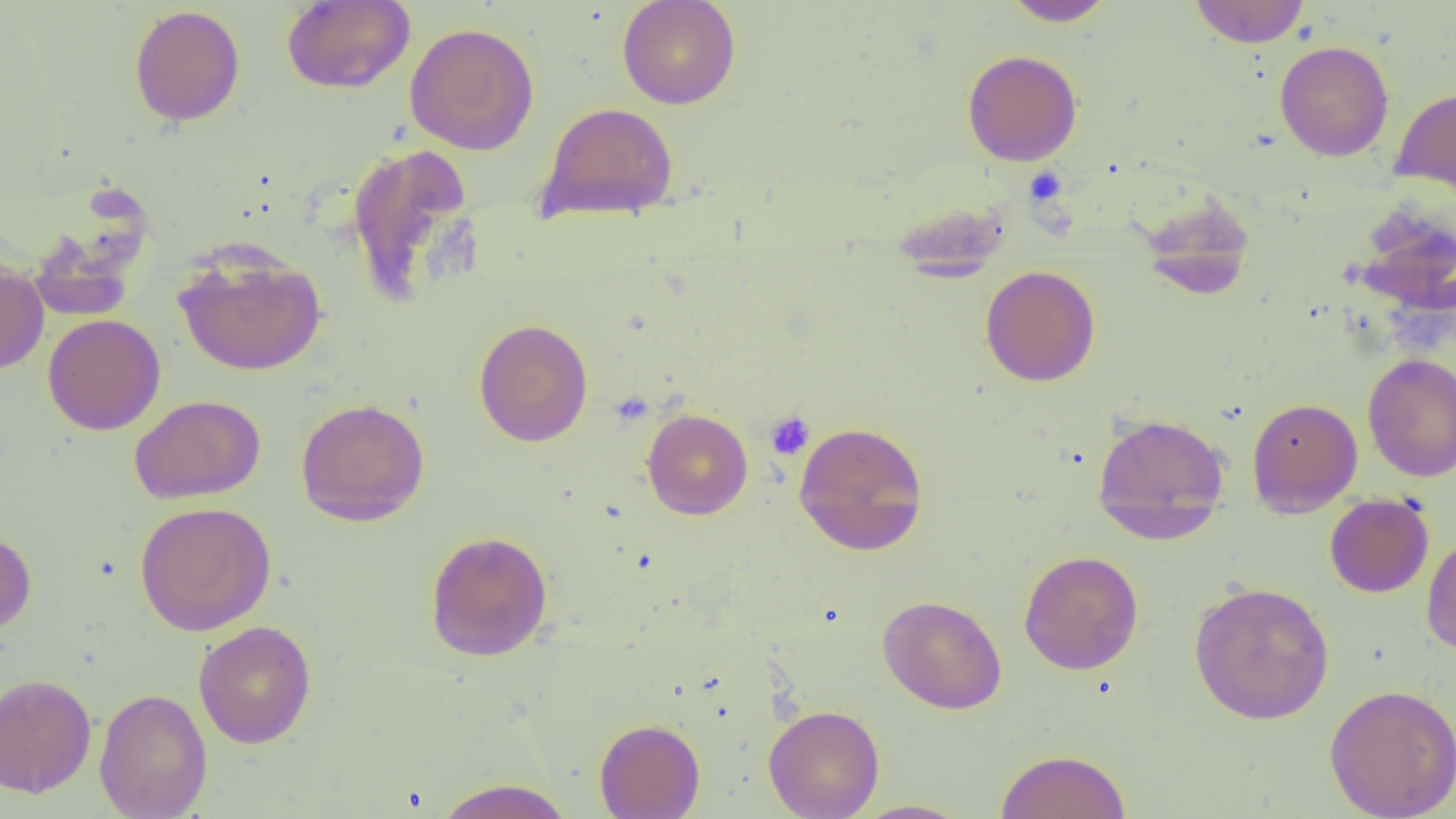
Summary:
  - Coordinate format: approximate bounding boxes as named x1/y1/x2/y2 corners in pixels
  - Platelet locations: (x1=1024, y1=167, x2=1068, y2=206), (x1=765, y1=411, x2=816, y2=461)
  - Uninfected red blood cell locations: (x1=617, y1=0, x2=741, y2=109), (x1=1002, y1=0, x2=1116, y2=26), (x1=1189, y1=0, x2=1311, y2=48), (x1=281, y1=1, x2=415, y2=93), (x1=129, y1=5, x2=245, y2=127), (x1=405, y1=22, x2=539, y2=155), (x1=1274, y1=40, x2=1394, y2=161), (x1=962, y1=49, x2=1083, y2=166), (x1=1391, y1=85, x2=1456, y2=200), (x1=536, y1=102, x2=679, y2=224), (x1=344, y1=142, x2=477, y2=306), (x1=1137, y1=191, x2=1256, y2=300), (x1=173, y1=243, x2=326, y2=376), (x1=0, y1=261, x2=49, y2=375), (x1=980, y1=265, x2=1100, y2=386), (x1=42, y1=314, x2=165, y2=435), (x1=473, y1=318, x2=593, y2=447), (x1=1363, y1=353, x2=1456, y2=482), (x1=130, y1=395, x2=266, y2=504), (x1=1247, y1=397, x2=1363, y2=516), (x1=296, y1=398, x2=430, y2=525), (x1=641, y1=408, x2=753, y2=519), (x1=1092, y1=412, x2=1230, y2=541), (x1=793, y1=420, x2=929, y2=556), (x1=1324, y1=493, x2=1434, y2=598), (x1=134, y1=501, x2=276, y2=636), (x1=0, y1=527, x2=36, y2=637), (x1=1421, y1=530, x2=1456, y2=656), (x1=425, y1=531, x2=553, y2=661), (x1=1019, y1=550, x2=1144, y2=675), (x1=1189, y1=581, x2=1335, y2=725), (x1=878, y1=595, x2=1007, y2=714), (x1=194, y1=620, x2=316, y2=749), (x1=0, y1=673, x2=98, y2=797), (x1=1324, y1=683, x2=1456, y2=819), (x1=94, y1=688, x2=212, y2=819), (x1=763, y1=704, x2=885, y2=819), (x1=594, y1=718, x2=705, y2=818), (x1=995, y1=748, x2=1131, y2=818), (x1=433, y1=778, x2=575, y2=819), (x1=850, y1=799, x2=972, y2=818)
  - Slide-level diagnosis: negative for blood parasites
  - Modality: light microscopy
  - Field of view: one of a larger specimen
  - Image size: 1456×819 pixels
  - Preparation: thin blood smear
  - Magnification: 1000x